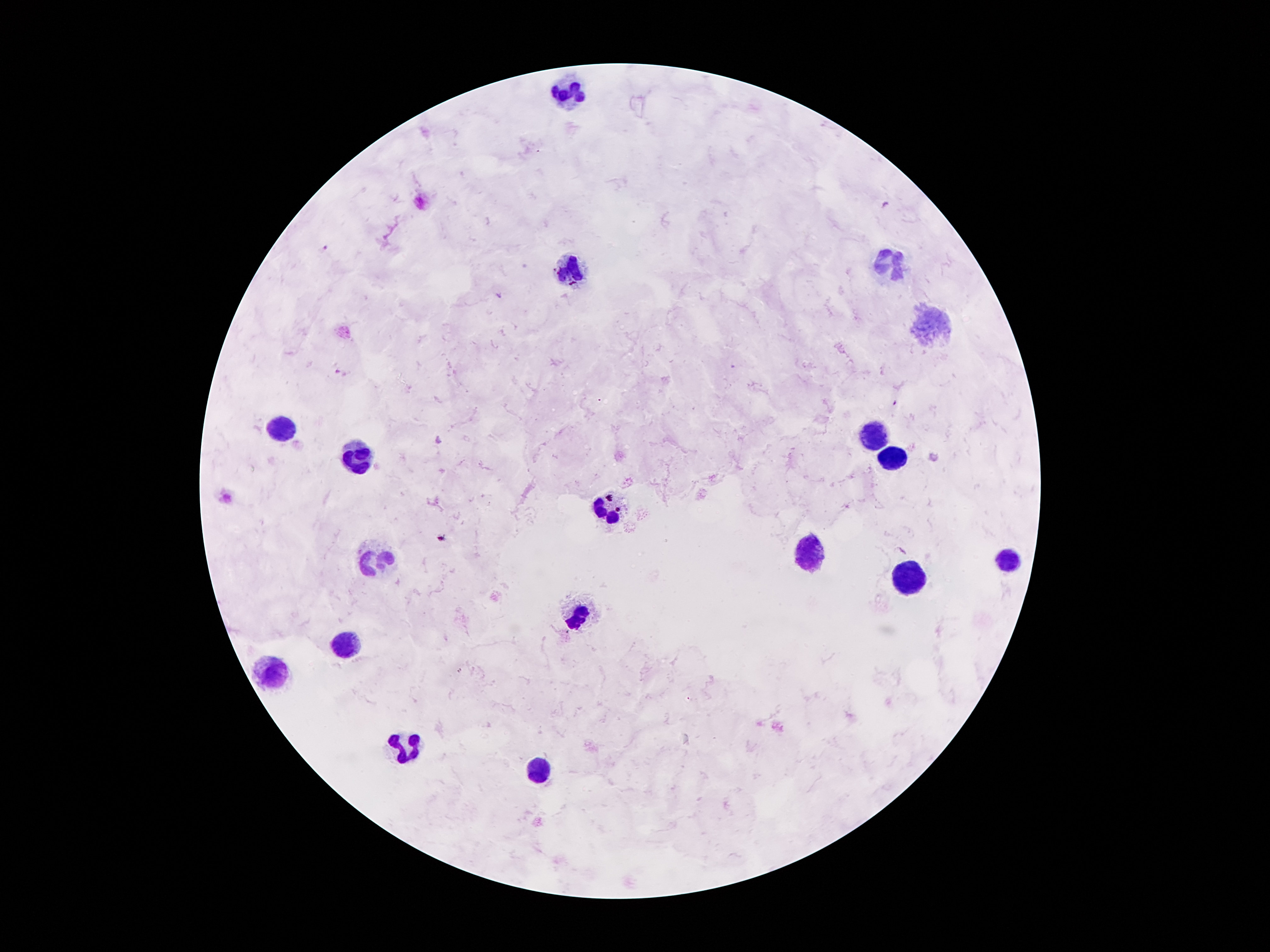
Approximate centers as {x, y} in pixels. Leukocyte locations: {568, 94}, {891, 258}, {568, 267}, {935, 324}, {283, 429}, {874, 434}, {358, 454}, {890, 459}, {607, 510}, {806, 553}, {374, 560}, {1008, 562}, {907, 583}, {578, 617}, {347, 646}, {268, 673}, {407, 748}, {537, 768}. Plasmodium parasite locations: {886, 206}, {323, 249}, {499, 295}, {341, 372}. Smartphone photograph taken through the microscope eyepiece. Single field of view. Thick blood smear. Image is 1270×952 pixels. Patient malaria status: positive for Plasmodium falciparum. 100x magnification. Giemsa-stained preparation.